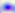

modality = micrograph
magnification = 400x
identification = Toxoplasma gondii